State the preparation type.
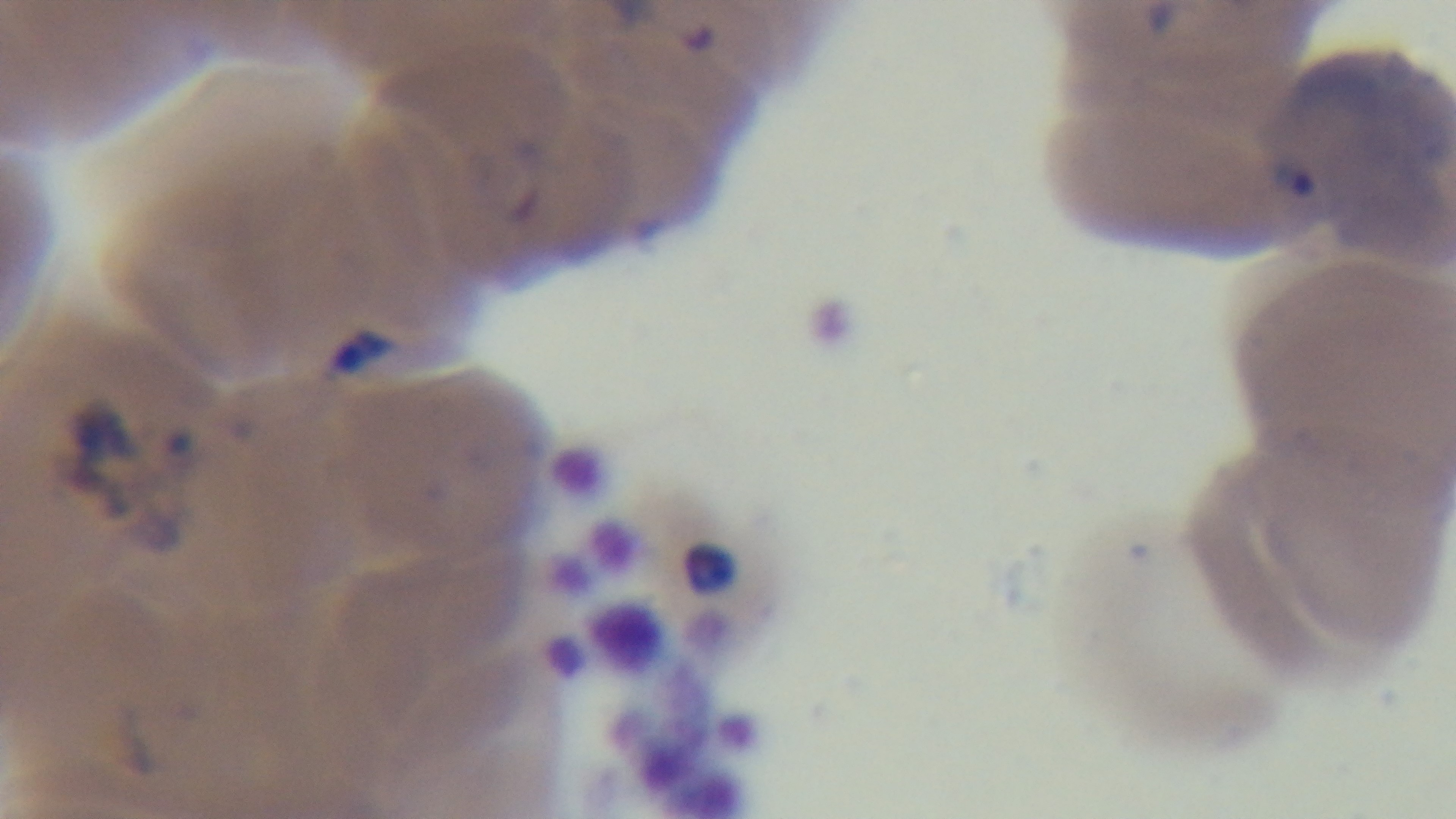

A thin smear.

Light microscopy. Captured with a mounted 4K digital camera. Giemsa stain. Malaria status: positive. 100x oil-immersion objective. Single field of view.